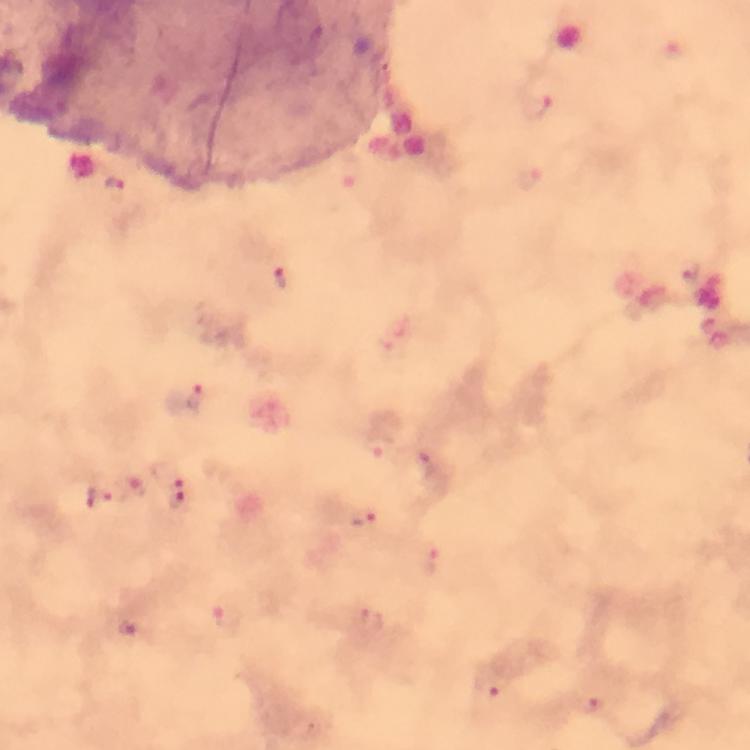

Approximate centers as [x, y] in pixels.
Summary:
  - Plasmodium parasite locations: [537, 107], [113, 187], [692, 272], [282, 280], [191, 398], [379, 445], [423, 459], [169, 475], [136, 488], [100, 497], [179, 499], [366, 516], [428, 559], [226, 617], [369, 620], [128, 629], [490, 685], [589, 705]
  - Immersion oil: applied
  - Stain: Giemsa
  - Cropped from: one field of view
  - Image size: 750×750 pixels
  - Magnification: 100x
  - Context: from a malaria diagnostic workup
  - Preparation: thick smear
  - Capture: smartphone photograph through a microscope